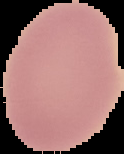
Summary:
  - Preparation: thin blood smear
  - Image type: segmented cell region on a black background
  - Image size: 124×154 pixels
  - Result: negative for malaria parasites